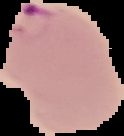
Malaria status: parasitized. Cell region segmented out of the field of view; the surrounding area is masked to black. From a thin blood film. Image is 124×136 pixels.